Outline each blood parasite and name the species.
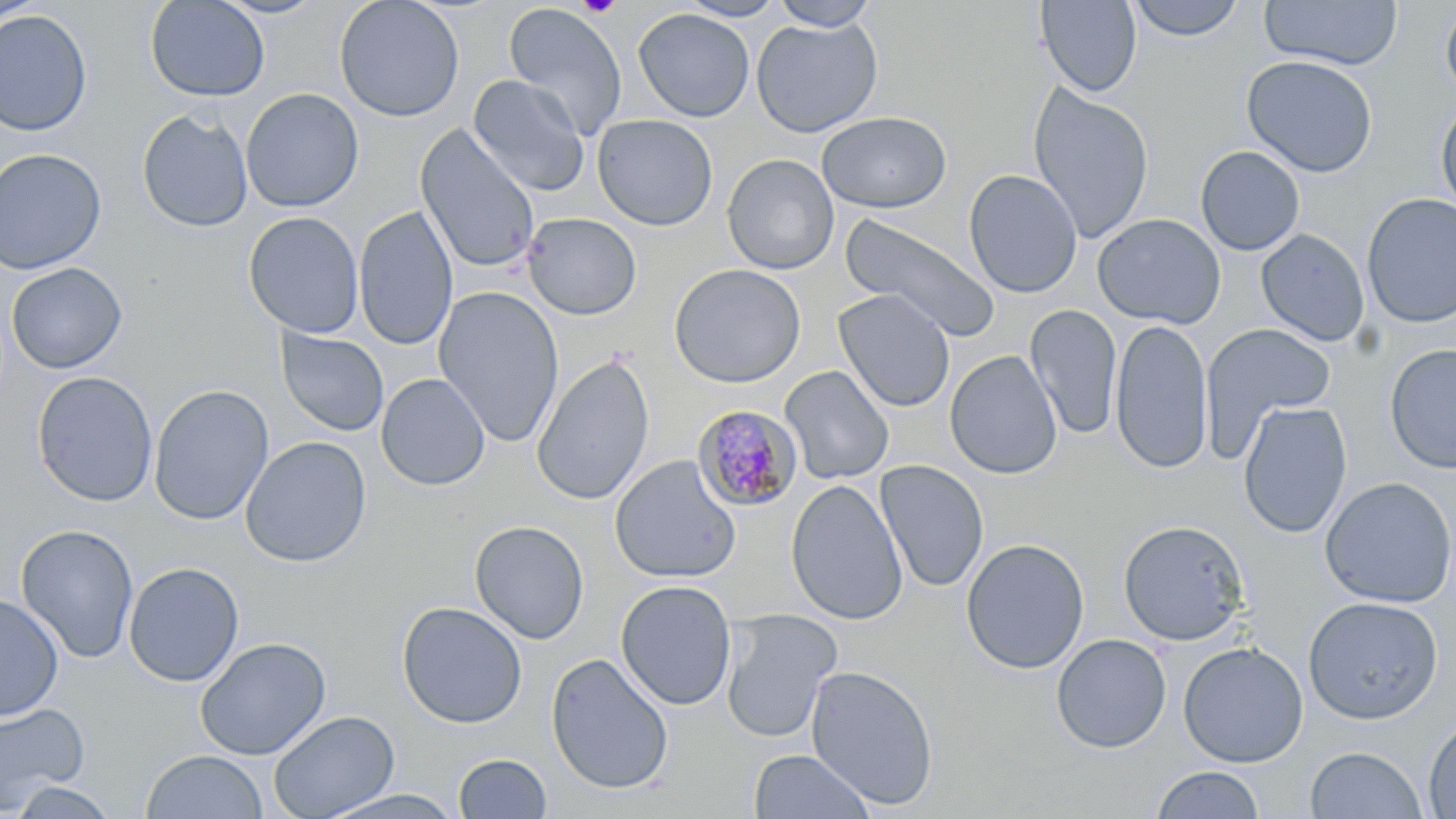
Approximate bounding boxes as (x1,y1)-(x2,y2) corner pairs in pixels.
Plasmodium malariae-infected red blood cells: (693,403)-(805,511).
No Plasmodium falciparum, Plasmodium ovale, Plasmodium vivax, Babesia divergens, or Trypanosoma brucei observed.

Uninfected red blood cell locations: (144,0)-(270,103), (211,0)-(329,20), (333,0)-(465,122), (675,0)-(789,21), (770,0)-(879,31), (1035,0)-(1143,97), (1128,0)-(1245,42), (1259,0)-(1403,70), (0,1)-(45,26), (503,2)-(627,140), (1440,2)-(1456,102), (633,8)-(755,122), (0,9)-(94,136), (751,16)-(883,138), (1241,54)-(1379,177), (468,74)-(590,197), (1028,84)-(1154,243), (241,87)-(364,213), (1435,98)-(1456,217), (137,109)-(253,233), (816,111)-(952,213), (592,114)-(718,231), (414,123)-(541,275), (1195,146)-(1305,256), (0,148)-(107,275), (721,153)-(839,275), (963,169)-(1083,298), (1361,193)-(1456,328), (354,206)-(458,352), (243,211)-(364,339), (841,212)-(1001,341), (522,213)-(642,321), (1092,214)-(1226,329), (1256,229)-(1370,347), (6,262)-(127,374), (668,263)-(806,388), (433,287)-(565,446), (832,289)-(956,413), (1025,304)-(1123,439), (1110,318)-(1214,474), (1199,324)-(1336,458), (276,327)-(390,437), (1384,344)-(1456,473), (944,350)-(1063,479), (532,353)-(655,506), (780,365)-(895,485), (32,371)-(158,507), (376,373)-(490,491), (149,385)-(274,525), (1238,401)-(1352,539), (240,436)-(372,567), (609,455)-(742,584), (874,460)-(989,593), (1319,476)-(1456,608), (786,479)-(907,625), (1117,519)-(1251,646), (470,520)-(590,644), (16,524)-(139,664), (960,537)-(1090,674), (123,561)-(245,687), (615,579)-(737,711), (0,593)-(64,722), (1302,596)-(1444,725), (396,601)-(528,728), (719,608)-(842,743), (1051,633)-(1172,753), (195,637)-(331,760), (1177,642)-(1309,767), (545,651)-(674,795), (805,664)-(939,810), (0,701)-(90,813), (267,710)-(400,819), (1422,716)-(1456,818), (1305,746)-(1428,818), (748,748)-(876,819), (141,750)-(268,819), (453,752)-(553,818), (1150,766)-(1266,819), (8,779)-(121,818), (317,789)-(465,818). Platelet locations: (575,0)-(623,17). Slide-level diagnosis: Plasmodium malariae. Single field of view. Captured at 1000x magnification. May-Grünwald-Giemsa stain. Image is 1456×819 pixels. Optical microscopy. Thin blood film.